Assess this cell for malaria.
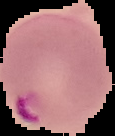

Parasitized.

Summary:
  - Image type: segmented cell region on a black background
  - Preparation: thin blood film
  - Image size: 115×136 pixels